State which cell type is depicted.
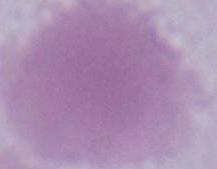

An erythrocyte.

magnification = 1000x
modality = photomicrograph